Classify the preparation.
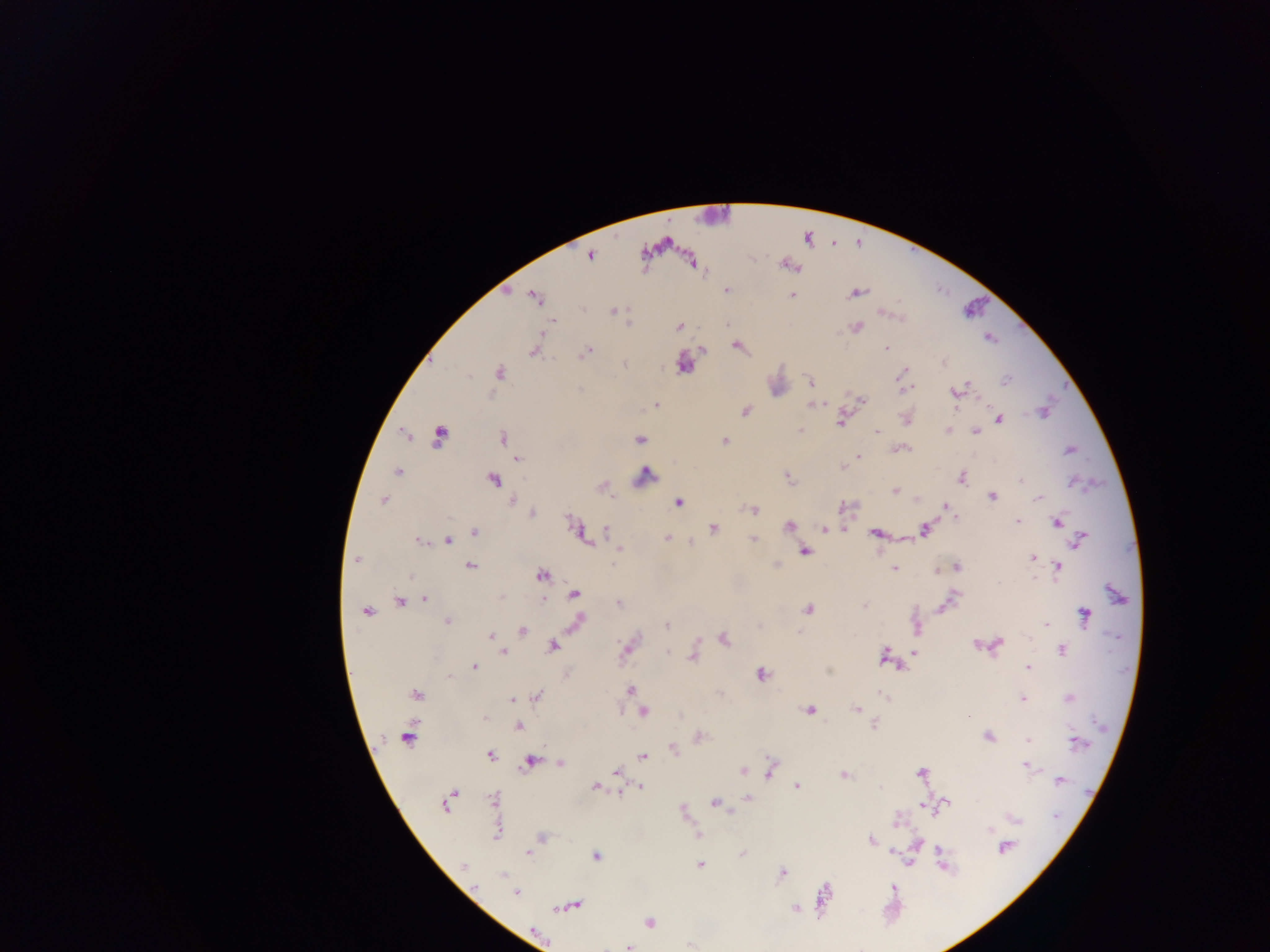

Thick blood film.

{
  "field_of_view": "single",
  "capture": "mobile-phone photograph through a microscope",
  "country": "Ghana",
  "plasmodium_parasite_locations": "approximate centers as [x, y] in pixels: [590, 255], [727, 290], [856, 292], [792, 295], [535, 297], [581, 308], [614, 310], [886, 314], [553, 321], [725, 323], [856, 326], [679, 327], [989, 338], [738, 347], [887, 348], [703, 349], [535, 351], [585, 352], [944, 363], [624, 365], [683, 365], [498, 372], [903, 373], [1005, 380], [810, 381], [904, 388], [579, 390], [955, 392], [862, 400], [656, 404], [813, 404], [745, 411], [1044, 412], [906, 419], [998, 420], [841, 421], [800, 429], [948, 429], [877, 431], [975, 433], [438, 437], [502, 437], [638, 439], [724, 441], [900, 449], [1069, 450], [858, 456], [518, 459], [843, 467], [398, 472], [645, 475], [962, 478], [494, 479], [789, 479], [1021, 480], [603, 486], [895, 491], [992, 496], [1039, 498], [382, 500], [512, 500], [678, 502], [947, 507], [752, 509], [532, 513], [954, 516], [569, 521], [1017, 522], [1057, 523], [788, 525], [714, 528], [844, 528], [823, 529], [924, 529], [606, 531], [474, 532], [874, 533], [667, 538], [753, 539], [1079, 539], [418, 541], [448, 541], [691, 543], [618, 549], [805, 552], [1032, 557], [356, 559], [776, 565], [471, 566], [957, 566], [1059, 566], [894, 569], [541, 575], [410, 577], [999, 582], [574, 594], [501, 597], [425, 598], [953, 598], [544, 599], [399, 602], [619, 603], [946, 603], [864, 605], [808, 609], [365, 612], [1085, 615], [447, 621], [577, 622], [1046, 624], [667, 626], [917, 629], [521, 630], [799, 633], [491, 636], [724, 640], [976, 644], [997, 645], [552, 647], [626, 648], [1061, 650], [503, 652], [916, 652], [668, 653], [884, 655], [693, 657], [475, 667], [1028, 668], [762, 675], [449, 676], [631, 689], [415, 694], [537, 695], [885, 696], [512, 698], [1069, 698], [1023, 699], [809, 709], [856, 709], [643, 712], [874, 725], [519, 726], [988, 736], [408, 737], [1028, 739], [1077, 742], [673, 749], [491, 755], [642, 756], [530, 761], [561, 763], [1026, 765], [771, 769], [616, 771], [743, 771], [921, 773], [844, 775], [1060, 780], [595, 786], [796, 786], [640, 787], [493, 798], [747, 798], [447, 803], [715, 803], [947, 803], [933, 807], [1056, 816], [1014, 818], [897, 821], [989, 830], [497, 833], [699, 835], [542, 838], [870, 841], [1005, 848], [942, 853], [528, 854], [743, 855], [596, 857], [700, 865], [463, 866], [782, 873], [503, 874], [893, 888], [516, 892], [823, 896], [572, 905], [795, 909], [649, 922], [628, 947]",
  "image_size": "1270×952 pixels"
}